State which parasite is depicted.
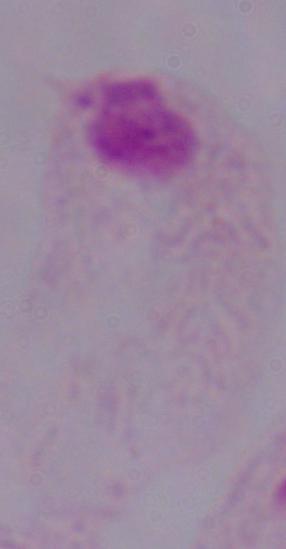
A trichomonad.

{
  "magnification": "1000x",
  "modality": "photomicrograph"
}